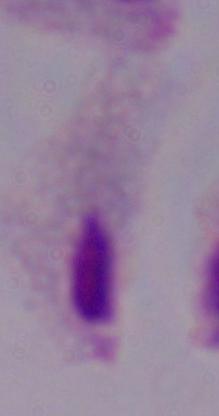
A trichomonad is seen. Captured at 1000x magnification. Micrograph.